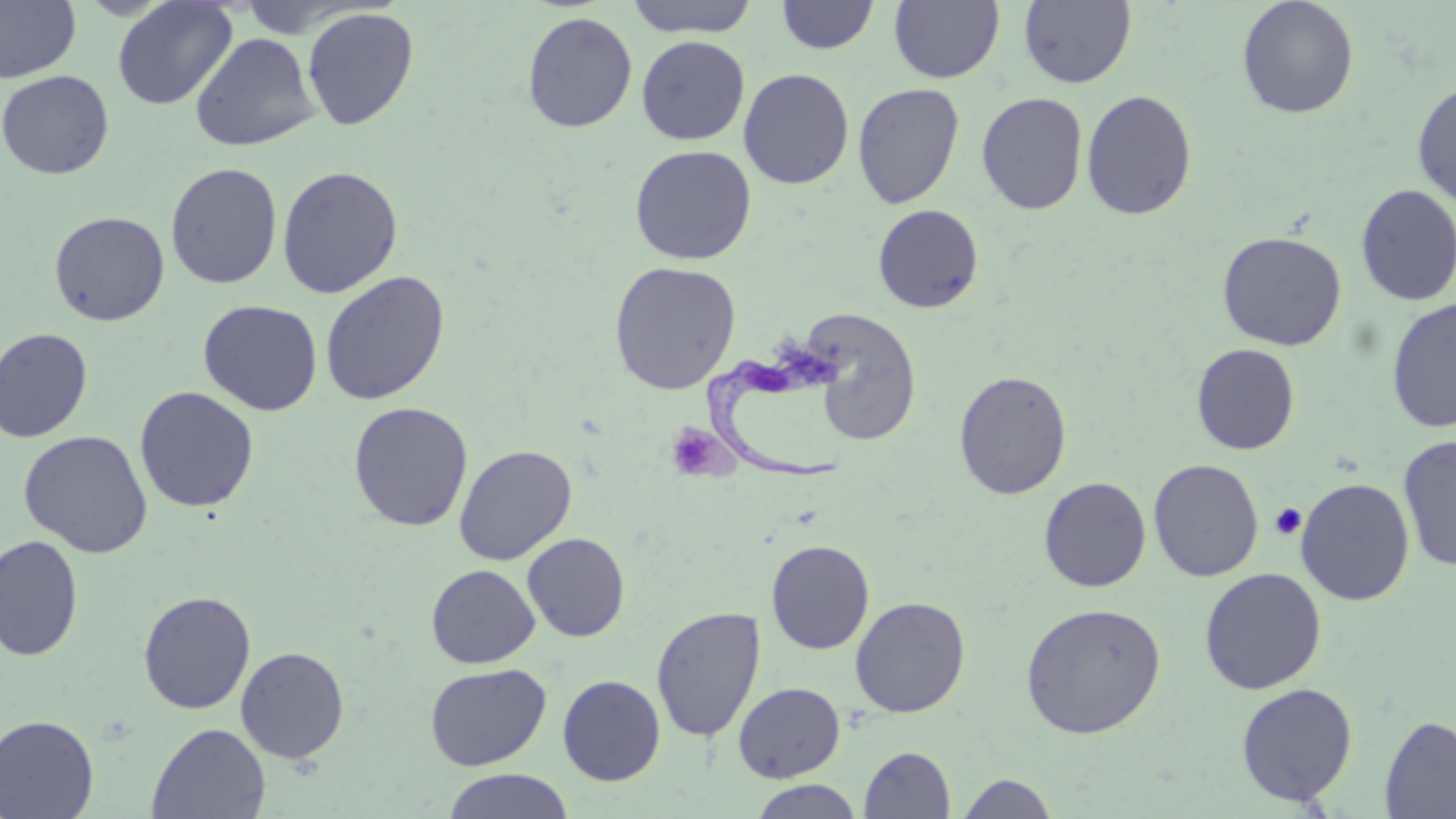
Summary:
  - Coordinate format: approximate bounding boxes as [x1, y1, x2, y2] in pixels
  - Uninfected red blood cell locations: [112, 0, 237, 110], [237, 0, 359, 36], [624, 0, 761, 37], [889, 0, 1004, 84], [1018, 0, 1136, 88], [1236, 0, 1359, 119], [0, 1, 81, 83], [776, 1, 880, 55], [302, 7, 419, 131], [521, 11, 637, 133], [190, 32, 320, 152], [636, 35, 750, 145], [738, 68, 854, 189], [0, 69, 115, 179], [1412, 80, 1456, 206], [852, 82, 964, 209], [1081, 89, 1198, 220], [976, 92, 1088, 215], [629, 144, 757, 265], [165, 161, 283, 289], [277, 165, 404, 298], [1355, 184, 1456, 306], [872, 204, 984, 314], [48, 211, 170, 326], [1217, 231, 1347, 351], [608, 261, 742, 395], [319, 270, 450, 406], [1385, 298, 1456, 433], [198, 299, 323, 415], [799, 307, 922, 446], [0, 327, 94, 443], [1191, 343, 1300, 455], [954, 369, 1072, 499], [134, 386, 259, 513], [348, 401, 473, 531], [18, 430, 153, 558], [1398, 434, 1456, 572], [453, 444, 577, 565], [1148, 459, 1264, 582], [1038, 476, 1151, 592], [1295, 477, 1415, 605], [522, 533, 630, 641], [0, 535, 83, 661], [766, 539, 875, 654], [426, 564, 540, 668], [1199, 567, 1327, 694], [138, 591, 256, 714], [850, 596, 971, 717], [1020, 602, 1166, 739], [651, 605, 766, 742], [235, 646, 350, 764], [425, 663, 551, 770], [557, 674, 666, 786], [733, 682, 845, 782], [1235, 682, 1358, 807], [0, 714, 99, 819], [1379, 715, 1456, 819], [147, 723, 270, 818], [859, 746, 955, 818], [441, 769, 575, 819], [956, 773, 1060, 818], [746, 779, 864, 818]
  - Platelet locations: [664, 422, 732, 482], [1270, 502, 1306, 540]
  - Trypanosoma brucei locations: [705, 341, 855, 486]
  - Slide-level diagnosis: Trypanosoma brucei
  - Modality: optical microscopy
  - Preparation: thin blood smear
  - Stain: May-Grünwald-Giemsa
  - Magnification: 1000x
  - Image size: 1456×819 pixels
  - Field of view: one of a larger specimen